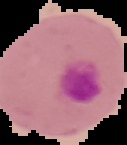 The area outside the segmented cell region is set to black. Malaria status: parasitized. Image is 127×145 pixels. From a thin blood smear.